Classify this cell by malaria status.
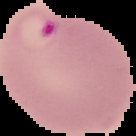
It is parasitized.

image type = segmented cell region on a black background
preparation = thin blood smear
image size = 136×136 pixels